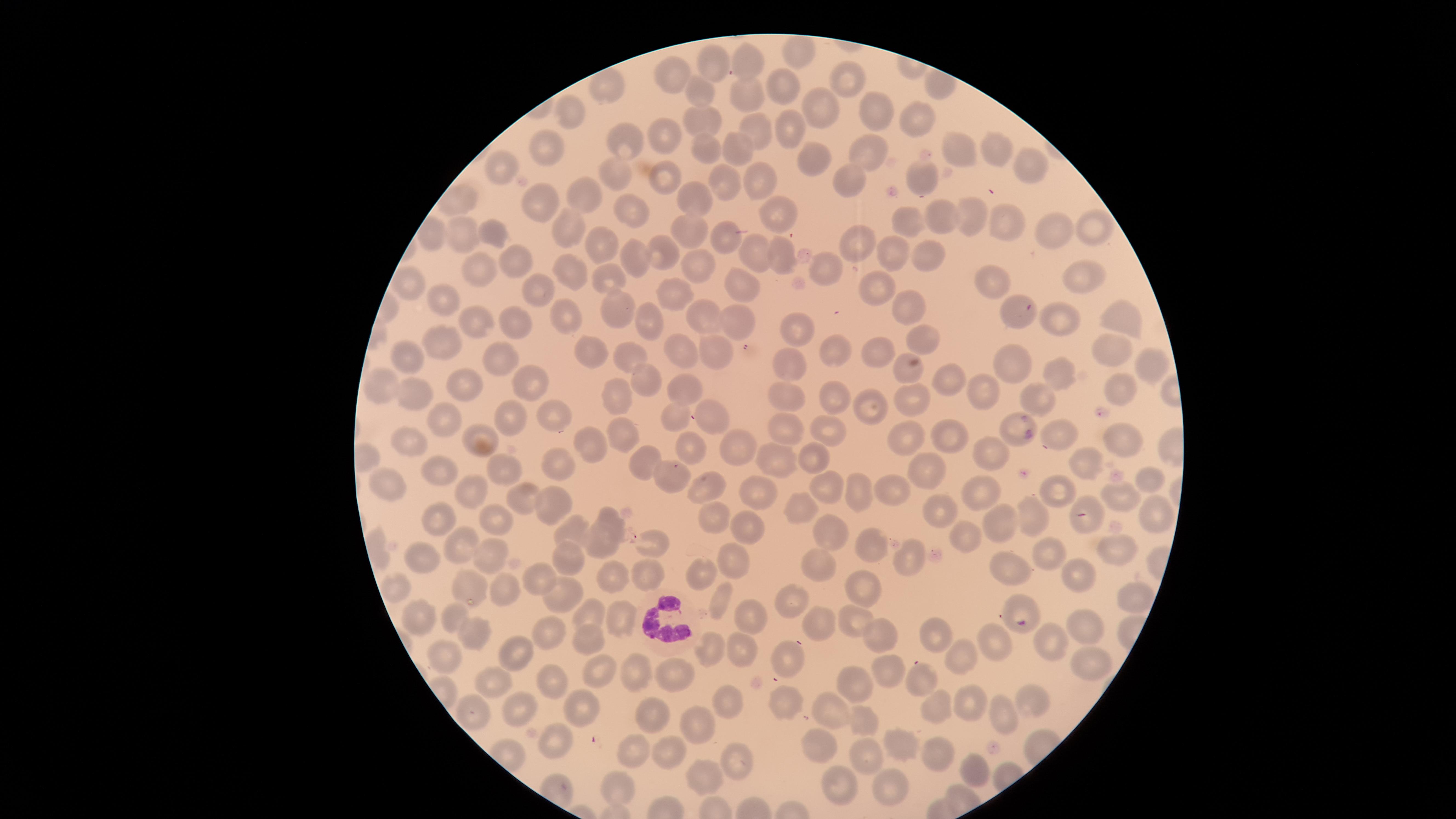
field_of_view: single
presence: no malaria parasites detected
visible_region: circular
capture: smartphone photograph through the microscope eyepiece
WBCs: 'approximate marker points, in pixels from the top-left corner: (x=661, y=621)'
uninfected_RBCs: 'approximate marker points, in pixels from the top-left corner: (x=798, y=54), (x=751, y=65), (x=707, y=66), (x=666, y=73), (x=779, y=81), (x=845, y=81), (x=600, y=90), (x=695, y=91), (x=741, y=93), (x=821, y=105), (x=874, y=113), (x=568, y=116), (x=701, y=117), (x=922, y=119), (x=784, y=121), (x=759, y=130), (x=667, y=136), (x=741, y=142), (x=623, y=143), (x=544, y=147), (x=996, y=147), (x=706, y=148), (x=956, y=150), (x=865, y=152), (x=814, y=159), (x=1034, y=165), (x=502, y=166), (x=615, y=172), (x=921, y=176), (x=663, y=180), (x=729, y=180), (x=759, y=180), (x=848, y=180), (x=689, y=195), (x=583, y=196), (x=542, y=205), (x=972, y=211), (x=632, y=215), (x=775, y=216), (x=938, y=216), (x=908, y=220), (x=999, y=223), (x=1093, y=227), (x=567, y=228), (x=694, y=228), (x=1048, y=232), (x=462, y=235), (x=857, y=237), (x=498, y=239), (x=723, y=240), (x=602, y=242), (x=887, y=249), (x=658, y=253), (x=513, y=257), (x=781, y=257), (x=754, y=259), (x=928, y=259), (x=640, y=260), (x=825, y=267), (x=690, y=268), (x=489, y=271), (x=572, y=276), (x=608, y=279), (x=1077, y=279), (x=990, y=281), (x=411, y=284), (x=748, y=285), (x=877, y=288), (x=534, y=292), (x=683, y=294), (x=441, y=307), (x=906, y=309), (x=1015, y=311), (x=610, y=313), (x=642, y=315), (x=565, y=319), (x=1120, y=319), (x=703, y=320), (x=1067, y=321), (x=473, y=322), (x=741, y=326), (x=515, y=334), (x=799, y=335), (x=918, y=339), (x=446, y=345), (x=833, y=347), (x=1112, y=348), (x=589, y=352), (x=880, y=353), (x=683, y=354), (x=713, y=354), (x=402, y=357), (x=626, y=358), (x=497, y=360), (x=1013, y=362), (x=1148, y=367), (x=789, y=369), (x=906, y=371), (x=1059, y=374), (x=946, y=379), (x=462, y=383), (x=644, y=383), (x=382, y=384), (x=527, y=384), (x=1122, y=388), (x=685, y=389), (x=616, y=392), (x=987, y=393), (x=409, y=395), (x=786, y=395), (x=1037, y=400), (x=838, y=401), (x=865, y=403), (x=912, y=403), (x=552, y=415), (x=706, y=417), (x=515, y=418), (x=670, y=419), (x=443, y=420), (x=621, y=428), (x=789, y=429), (x=1013, y=429), (x=828, y=430), (x=954, y=435), (x=1063, y=435), (x=481, y=436), (x=410, y=440), (x=742, y=441), (x=1127, y=441), (x=911, y=442), (x=587, y=443), (x=688, y=445), (x=772, y=455), (x=812, y=455), (x=990, y=457), (x=648, y=462), (x=554, y=466), (x=439, y=470), (x=505, y=470), (x=1086, y=470), (x=668, y=472), (x=927, y=477), (x=1149, y=482), (x=703, y=488), (x=756, y=488), (x=389, y=489), (x=978, y=489), (x=826, y=490), (x=860, y=490), (x=891, y=490), (x=1061, y=492), (x=462, y=493), (x=522, y=497), (x=1122, y=501), (x=545, y=505), (x=801, y=507), (x=940, y=507), (x=612, y=515), (x=1154, y=516), (x=1032, y=518), (x=434, y=519), (x=719, y=519), (x=493, y=521), (x=1088, y=521), (x=1004, y=525), (x=572, y=529), (x=741, y=529), (x=825, y=533), (x=961, y=535), (x=603, y=541), (x=650, y=543), (x=865, y=544), (x=1112, y=547), (x=463, y=548), (x=568, y=552), (x=486, y=554), (x=1049, y=555), (x=427, y=557), (x=731, y=557), (x=907, y=559), (x=652, y=567), (x=817, y=568), (x=1006, y=569), (x=701, y=572), (x=1078, y=574), (x=537, y=578), (x=608, y=579), (x=472, y=584), (x=864, y=585), (x=396, y=589), (x=506, y=591), (x=565, y=591), (x=721, y=599), (x=1121, y=600), (x=791, y=603), (x=1018, y=609), (x=417, y=614), (x=589, y=614), (x=753, y=617), (x=452, y=618), (x=621, y=621), (x=855, y=621), (x=824, y=624), (x=549, y=626), (x=1088, y=626), (x=937, y=632), (x=470, y=638), (x=877, y=638), (x=593, y=639), (x=993, y=643), (x=1048, y=643), (x=713, y=650), (x=518, y=651), (x=447, y=654), (x=953, y=656), (x=745, y=657), (x=781, y=657), (x=1088, y=663), (x=884, y=668), (x=598, y=671), (x=636, y=674), (x=672, y=674), (x=918, y=677), (x=549, y=680), (x=496, y=683), (x=859, y=684), (x=1027, y=698), (x=725, y=700), (x=932, y=703), (x=575, y=706), (x=520, y=707), (x=784, y=709), (x=835, y=710), (x=971, y=710), (x=471, y=714), (x=642, y=715), (x=1003, y=718), (x=871, y=724), (x=695, y=726), (x=552, y=741), (x=904, y=745), (x=813, y=749), (x=632, y=753), (x=670, y=753), (x=939, y=756), (x=870, y=758), (x=737, y=761), (x=972, y=770), (x=704, y=781), (x=893, y=789), (x=618, y=790), (x=845, y=794)'
stain: Giemsa
preparation: thin blood smear
image_size: 1456×819 pixels